Classify this cell by malaria status.
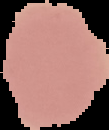

It is uninfected.

{
  "image_type": "segmented cell region with the area outside set to black",
  "preparation": "thin blood film",
  "image_size": "109×130 pixels"
}